Report the malaria status of this cell.
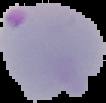
Parasitized.

The area outside the segmented cell region is set to black. From a thin blood film. Image is 106×103 pixels.